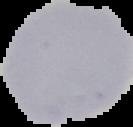 From a thin blood film. Malaria status: uninfected. Segmented cell region on a black background. Image is 133×127 pixels.